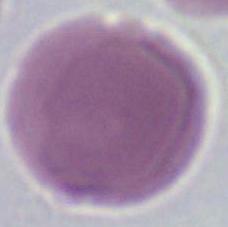

Captured at 1000x magnification. Micrograph. A red blood cell is seen.